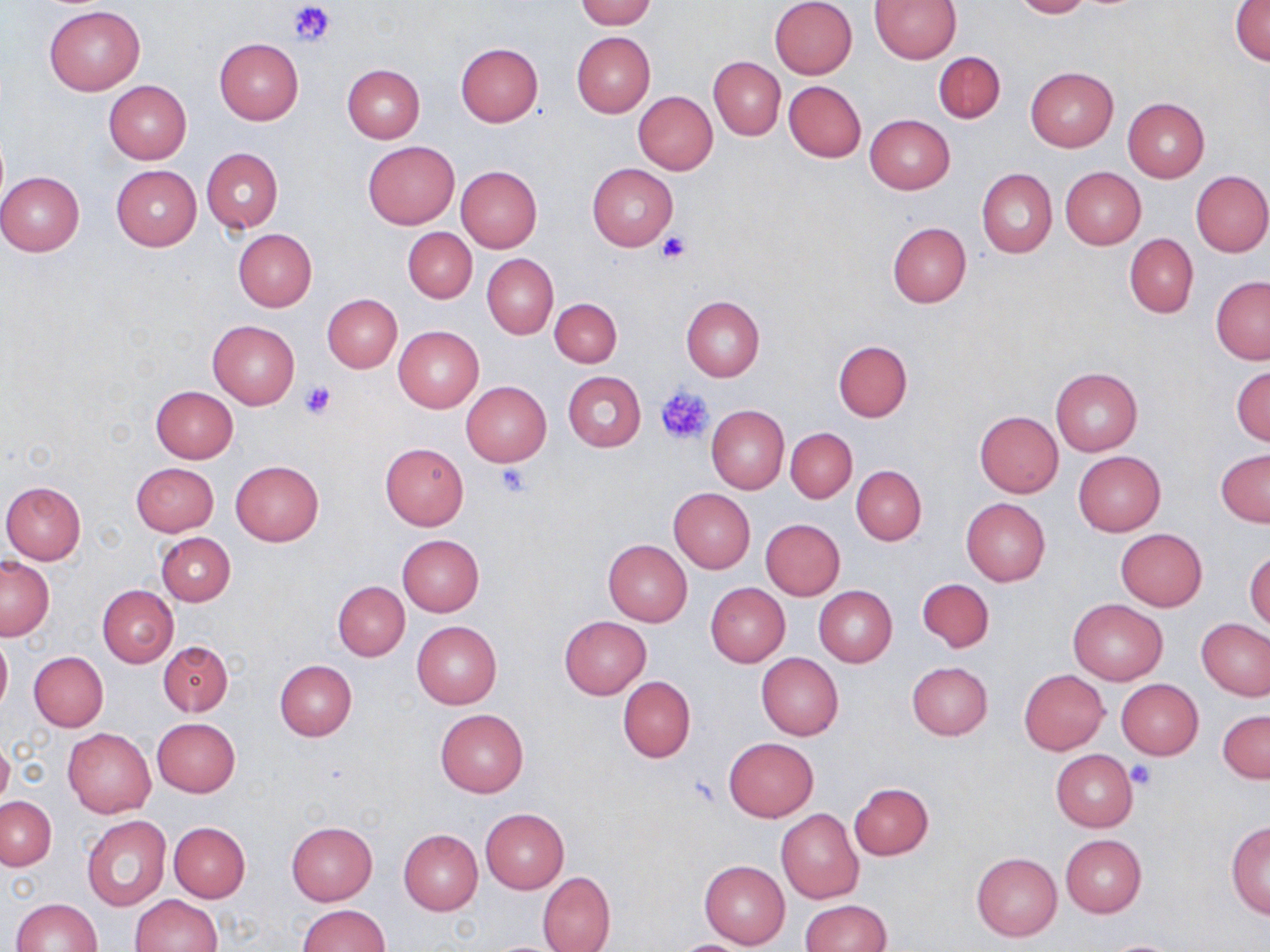
slide-level diagnosis = negative for blood parasites
platelet locations = approximate bounding boxes as [x1, y1, x2, y2] in pixels: [288, 1, 335, 48], [657, 233, 690, 264], [299, 380, 338, 419], [656, 386, 715, 446], [494, 464, 532, 497], [1127, 761, 1155, 789], [685, 775, 720, 807]
preparation = thin blood smear
modality = light microscopy
field of view = single
stain = May-Grünwald-Giemsa
image size = 1270×952 pixels
magnification = 1000x
uninfected red blood cell locations = approximate bounding boxes as [x1, y1, x2, y2] in pixels: [577, 0, 655, 27], [770, 0, 857, 79], [871, 0, 960, 64], [1012, 0, 1090, 18], [1232, 2, 1270, 66], [43, 6, 144, 95], [572, 32, 656, 117], [214, 38, 303, 124], [455, 42, 542, 127], [933, 52, 1005, 122], [708, 57, 785, 139], [343, 64, 425, 143], [1025, 67, 1119, 152], [103, 80, 191, 164], [783, 81, 866, 162], [633, 91, 717, 174], [1122, 97, 1210, 182], [865, 114, 954, 194], [362, 141, 459, 229], [201, 147, 282, 232], [588, 164, 677, 250], [112, 165, 201, 250], [456, 166, 541, 253], [1060, 167, 1145, 249], [976, 168, 1057, 257], [1191, 170, 1270, 257], [1, 172, 84, 256], [887, 222, 972, 307], [233, 228, 317, 311], [403, 228, 477, 302], [1125, 233, 1198, 317], [481, 254, 558, 339], [1211, 277, 1270, 365], [322, 294, 402, 373], [681, 296, 764, 380], [550, 297, 621, 368], [208, 320, 299, 407], [394, 326, 483, 412], [834, 340, 912, 421], [1232, 366, 1270, 446], [1051, 367, 1143, 455], [564, 372, 646, 451], [461, 382, 551, 467], [150, 386, 238, 462], [707, 404, 788, 494], [974, 411, 1064, 498], [786, 429, 857, 502], [380, 442, 469, 529], [1216, 448, 1270, 527], [1072, 452, 1166, 537], [230, 460, 324, 546], [130, 462, 219, 537], [851, 466, 926, 545], [1, 480, 87, 564], [669, 489, 755, 573], [961, 498, 1050, 586], [760, 518, 846, 600], [1116, 528, 1208, 611], [156, 533, 234, 606], [398, 535, 484, 615], [602, 540, 692, 627], [1245, 550, 1270, 632], [1, 557, 53, 640], [917, 578, 994, 652], [333, 582, 409, 661], [705, 583, 790, 667], [98, 585, 178, 666], [813, 586, 897, 666], [1067, 597, 1168, 685], [559, 616, 651, 699], [1196, 617, 1269, 701], [412, 622, 502, 708], [0, 633, 11, 716], [158, 640, 233, 716], [27, 651, 108, 731], [756, 653, 843, 741], [274, 660, 356, 741], [907, 662, 993, 740], [1019, 669, 1109, 754], [618, 677, 696, 762], [1115, 679, 1204, 759], [434, 708, 528, 797], [1218, 710, 1270, 784], [152, 718, 239, 797], [63, 728, 155, 818], [723, 738, 819, 822], [0, 739, 13, 811], [1050, 750, 1138, 831], [849, 783, 933, 860], [1, 797, 56, 870], [480, 809, 570, 893], [776, 809, 864, 904], [82, 815, 171, 912], [286, 821, 377, 904], [169, 822, 251, 902], [1226, 822, 1269, 917], [399, 829, 483, 916], [1061, 834, 1145, 917], [971, 852, 1062, 941], [699, 860, 790, 948], [537, 871, 616, 952], [132, 894, 222, 952], [12, 898, 102, 951], [799, 900, 890, 952], [297, 904, 390, 952], [1101, 938, 1183, 951], [667, 939, 762, 952]